Identify the blood parasite species.
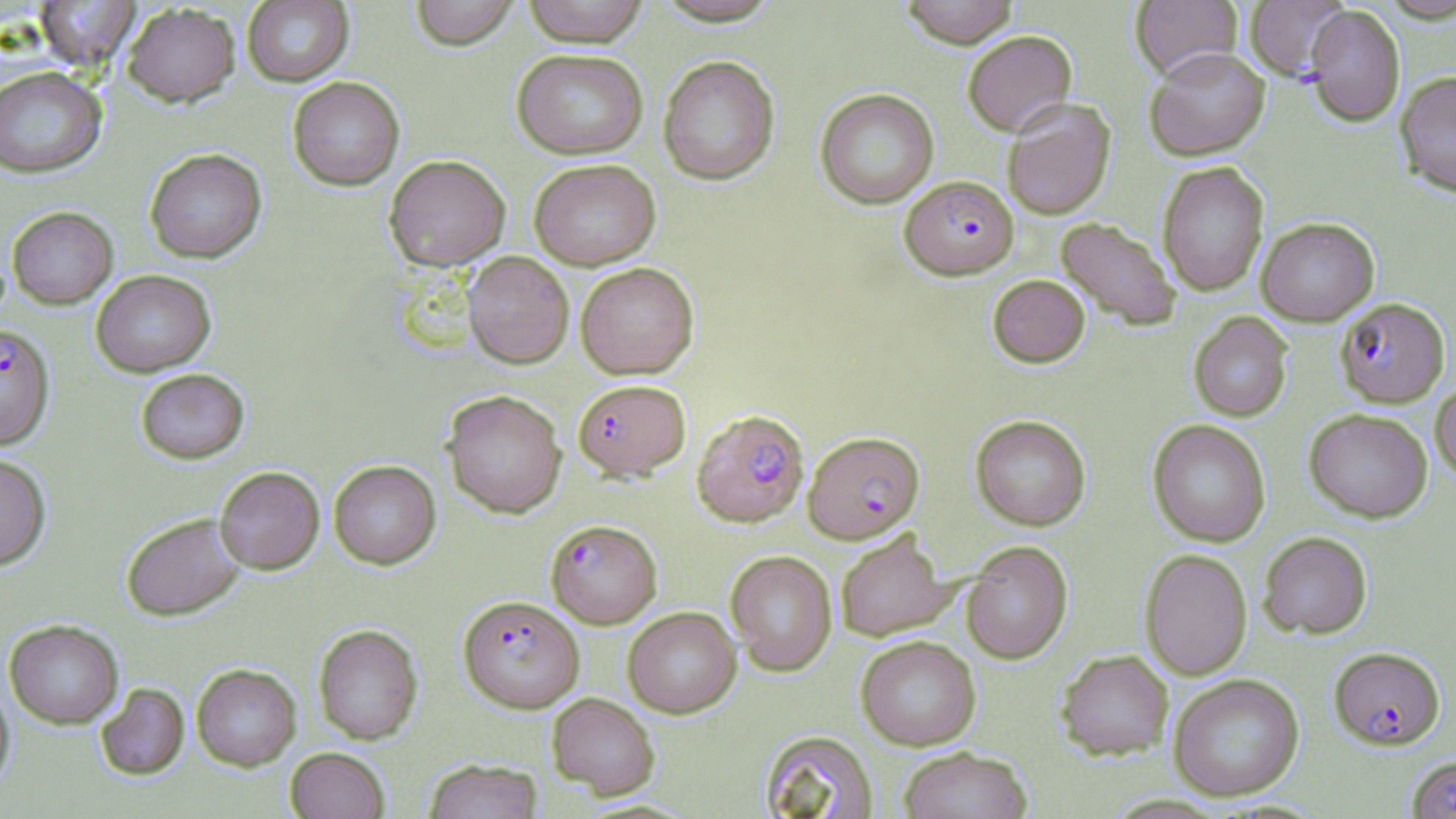
Plasmodium falciparum.

Summary:
  - Coordinate format: approximate bounding boxes as (x1,y1)-(x2,y2) corner pairs in pixels
  - Plasmodium falciparum-infected red blood cell locations (subset): (900,175)-(1019,280), (1335,297)-(1450,408), (0,323)-(56,450), (572,378)-(691,481), (692,409)-(809,527), (803,431)-(924,543), (545,519)-(662,628), (458,595)-(585,713), (1329,647)-(1445,750)
  - Uninfected red blood cell locations (subset): (409,0)-(521,50), (520,0)-(650,47), (899,0)-(1019,48), (1130,0)-(1242,80), (1244,0)-(1350,82), (33,1)-(141,70), (241,1)-(354,87), (121,2)-(240,107), (1304,5)-(1405,127), (962,30)-(1077,135), (1144,47)-(1271,161), (511,48)-(649,160), (658,55)-(780,186), (0,66)-(107,178), (1395,70)-(1456,197), (287,77)-(404,191), (815,88)-(939,208), (1002,98)-(1116,220), (144,148)-(267,263), (384,154)-(511,271), (529,159)-(661,271), (1157,161)-(1269,296), (7,206)-(118,309), (1255,216)-(1380,326), (1055,217)-(1182,331), (463,251)-(574,368), (575,262)-(699,379), (91,269)-(216,377), (988,274)-(1090,368), (1189,312)-(1293,422), (136,368)-(249,463), (1430,380)-(1456,483), (441,390)-(567,518), (1304,408)-(1433,523), (969,414)-(1091,530), (1147,419)-(1271,547), (0,453)-(51,570), (329,459)-(441,569), (215,466)-(325,574), (121,513)-(246,620), (834,529)-(957,642), (1258,531)-(1372,639), (961,540)-(1073,664), (1139,549)-(1252,680), (725,550)-(838,676), (623,606)-(741,718), (4,619)-(124,729), (313,624)-(423,745), (855,635)-(981,750), (1055,649)-(1174,760), (191,664)-(301,771), (1168,673)-(1304,801), (0,677)-(15,797), (95,682)-(190,781), (547,692)-(660,799), (758,730)-(879,818), (285,747)-(390,819), (897,747)-(1032,819), (424,758)-(543,819)
  - Stain: May-Grünwald-Giemsa
  - Modality: optical microscopy
  - Magnification: 1000x
  - Image size: 1456×819 pixels
  - Field of view: single
  - Preparation: thin blood film